Classify this cell by malaria status.
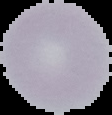

It is uninfected.

preparation = thin blood film
image size = 112×115 pixels
image type = segmented cell region on a black background